Point out each leukocyte.
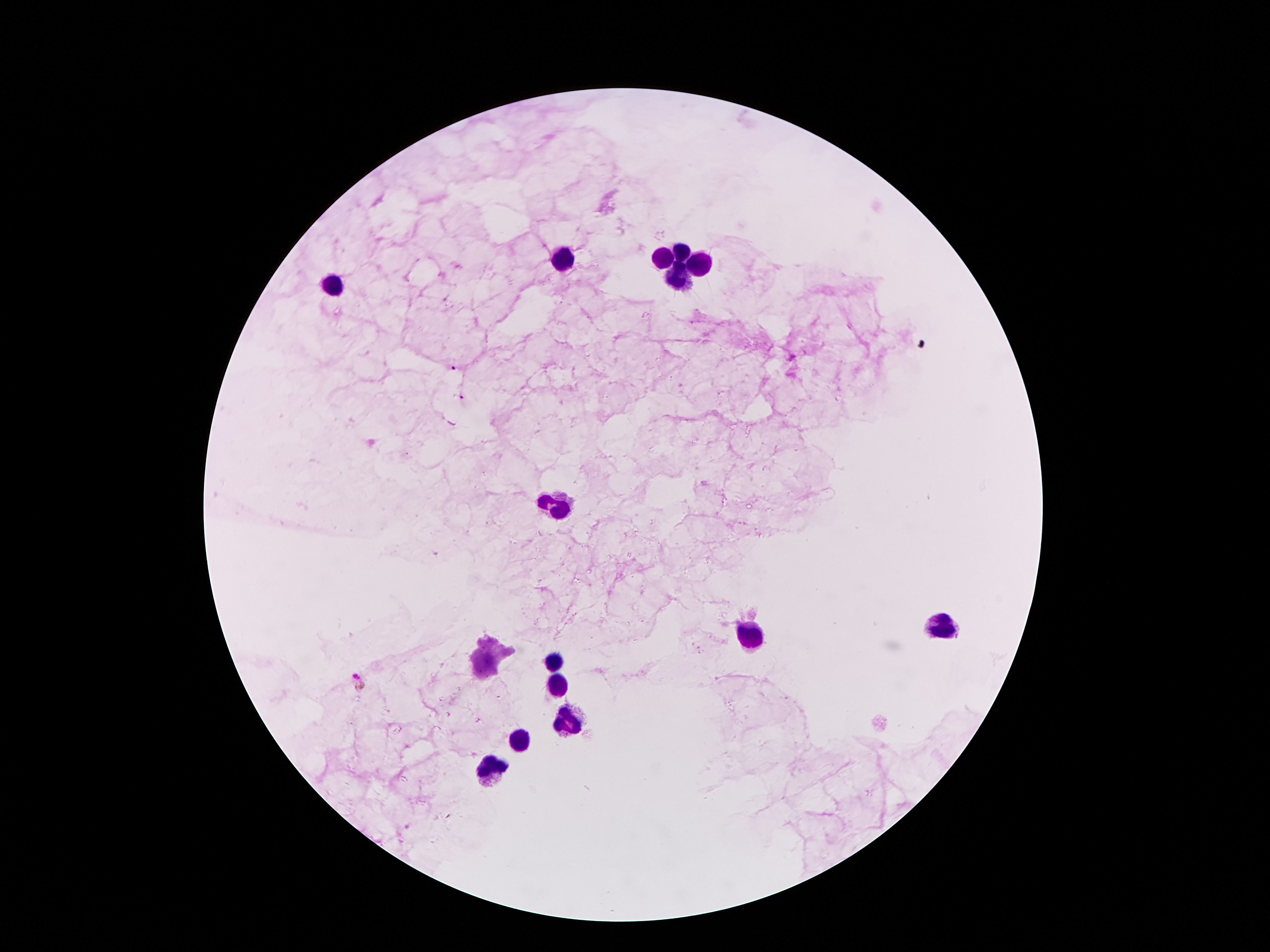

Approximate object centers, in pixels from the top-left corner.
Leukocytes: (x=684, y=251), (x=665, y=259), (x=567, y=261), (x=697, y=267), (x=676, y=278), (x=334, y=286), (x=558, y=508), (x=943, y=624), (x=751, y=631), (x=556, y=664), (x=560, y=683), (x=575, y=721), (x=519, y=740), (x=491, y=774).

malaria parasite locations = (x=453, y=368), (x=460, y=396), (x=358, y=680)
magnification = 100x
capture = smartphone through the microscope eyepiece
image size = 1270×952 pixels
stain = Giemsa
field of view = single
preparation = thick blood smear
patient malaria status = positive for Plasmodium falciparum